Classify this cell by malaria status.
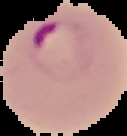

Parasitized.

{
  "image_size": "127×136 pixels",
  "image_type": "segmented cell region on a black background",
  "preparation": "thin blood film"
}